Classify this cell by malaria status.
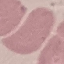

It is uninfected.

Summary:
  - Image type: cell patch, automatically extracted from a larger field of view and resized to 64 × 64 pixels
  - Stain: Giemsa
  - Capture: smartphone through the microscope eyepiece
  - Preparation: thin blood film